Outline each Plasmodium falciparum-infected red blood cell.
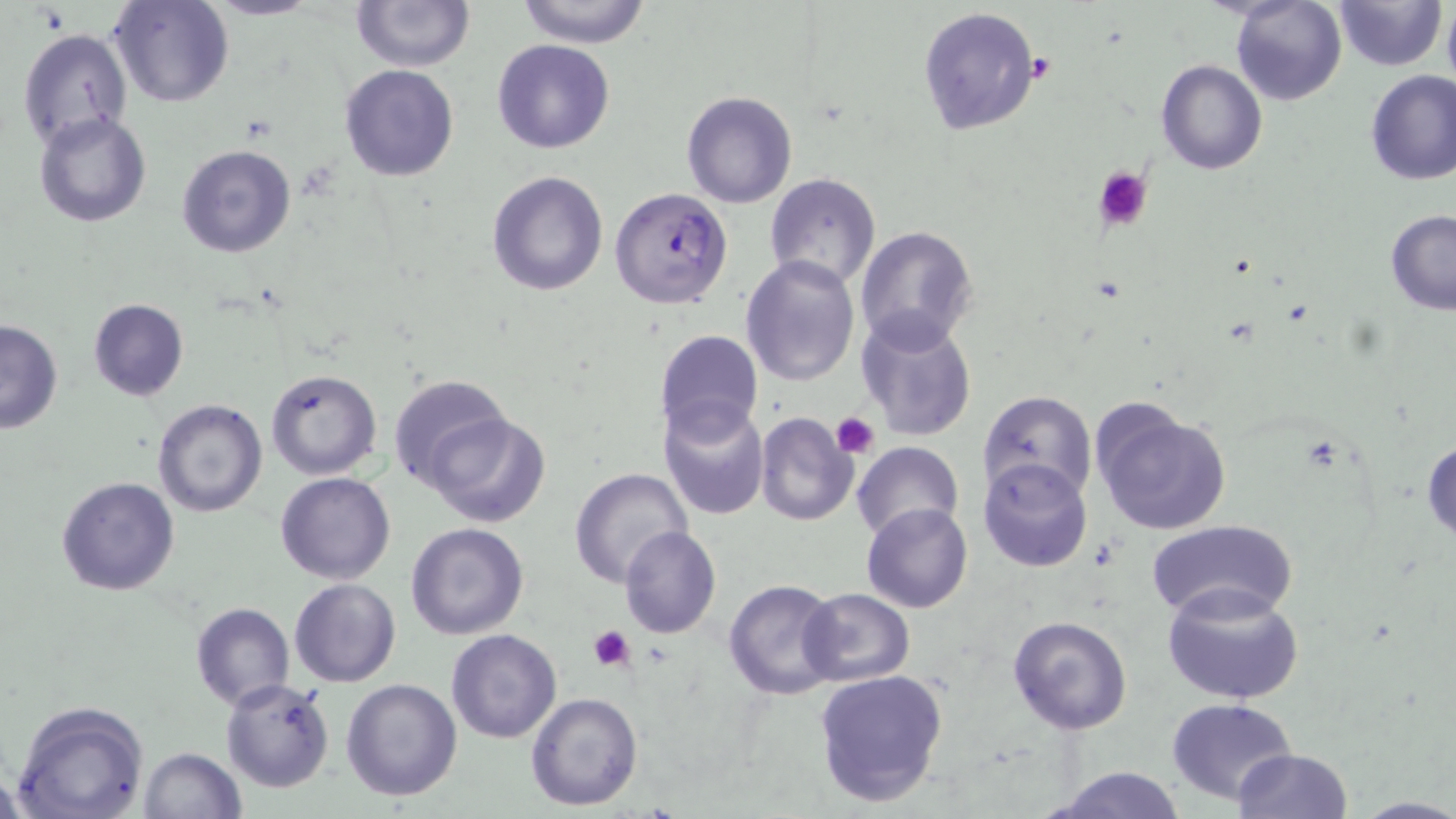
Approximate bounding boxes as [x1, y1, x2, y2] in pixels.
Plasmodium falciparum-infected red blood cells: [610, 187, 733, 309].

{
  "slide_level_diagnosis": "Plasmodium falciparum",
  "preparation": "thin blood smear",
  "modality": "light microscopy",
  "platelet_locations": "approximate bounding boxes as [x1, y1, x2, y2] in pixels: [1093, 166, 1153, 232], [832, 412, 880, 459], [588, 625, 637, 671]",
  "magnification": "1000x",
  "image_size": "1456×819 pixels",
  "uninfected_red_blood_cell_locations": "approximate bounding boxes as [x1, y1, x2, y2] in pixels: [109, 0, 235, 108], [203, 0, 320, 21], [352, 0, 474, 71], [516, 0, 652, 46], [1230, 0, 1346, 105], [1334, 1, 1445, 72], [918, 6, 1039, 137], [1442, 6, 1456, 88], [16, 26, 133, 150], [492, 39, 615, 153], [1157, 59, 1267, 175], [340, 63, 460, 182], [1364, 69, 1456, 185], [681, 91, 797, 208], [33, 110, 154, 228], [177, 144, 298, 259], [486, 169, 609, 296], [764, 173, 881, 290], [1384, 211, 1456, 314], [855, 225, 978, 350], [740, 256, 861, 386], [87, 298, 189, 401], [855, 310, 978, 443], [0, 320, 63, 434], [654, 328, 764, 442], [265, 369, 381, 479], [387, 373, 511, 492], [979, 391, 1096, 503], [151, 399, 269, 518], [658, 401, 771, 522], [1088, 401, 1233, 537], [755, 412, 859, 527], [427, 413, 551, 527], [1423, 435, 1456, 547], [851, 441, 963, 544], [977, 458, 1093, 572], [568, 467, 693, 585], [277, 472, 396, 585], [56, 476, 180, 595], [862, 503, 973, 614], [1147, 519, 1297, 622], [405, 522, 529, 639], [618, 525, 721, 639], [289, 578, 400, 687], [722, 579, 842, 700], [1161, 583, 1305, 706], [798, 588, 916, 688], [189, 601, 295, 711], [1007, 615, 1132, 734], [447, 629, 562, 743], [812, 668, 951, 810], [220, 678, 336, 794], [340, 678, 464, 801], [525, 691, 644, 811], [1166, 697, 1298, 803], [10, 701, 151, 819], [138, 748, 247, 819], [1232, 748, 1352, 818], [1046, 766, 1190, 819], [1353, 797, 1456, 818]",
  "stain": "May-Grünwald-Giemsa",
  "field_of_view": "single"
}